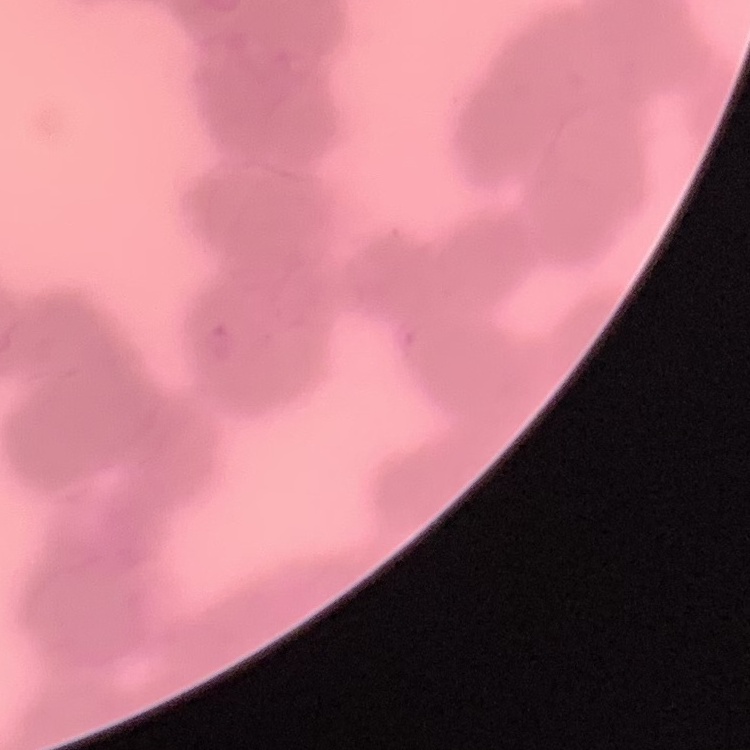

Summary:
  - Erythrocyte morphology: rouleaux formation
  - Image type: square crop of a larger photomicrograph
  - Stain: Field's or Giemsa
  - Preparation: thin peripheral smear